Identify the blood parasite species.
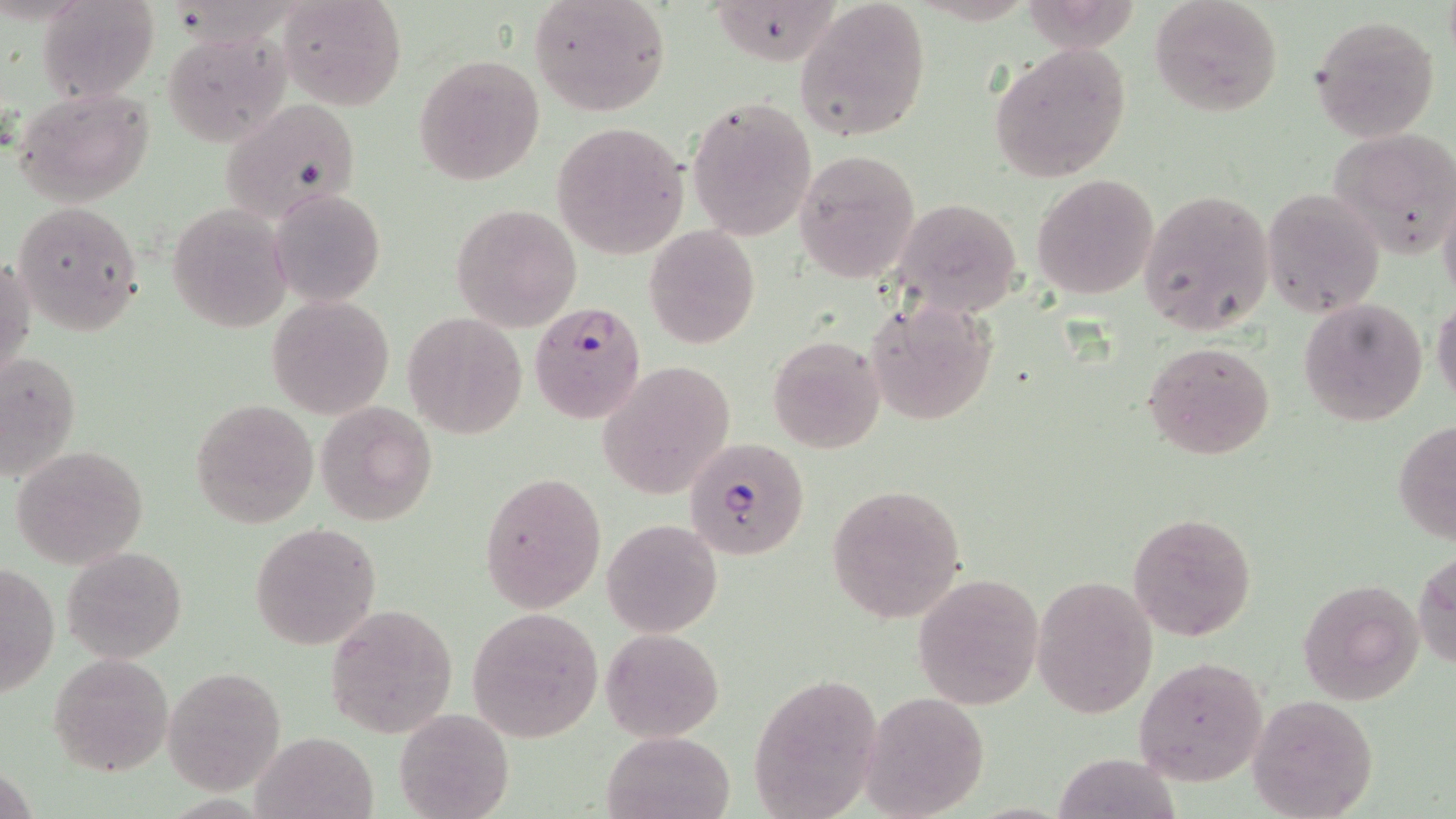
Plasmodium falciparum.

Approximate bounding boxes as [x1, y1, x2, y2] in pixels. Plasmodium falciparum-infected red blood cell locations: [529, 301, 648, 423], [686, 436, 811, 558]. Uninfected red blood cell locations: [280, 0, 406, 112], [528, 0, 673, 116], [793, 0, 931, 142], [1149, 0, 1284, 117], [38, 2, 156, 101], [1310, 16, 1440, 141], [163, 31, 289, 147], [989, 40, 1133, 182], [413, 54, 545, 185], [12, 86, 156, 207], [685, 97, 815, 241], [220, 98, 365, 223], [552, 124, 688, 257], [1327, 127, 1456, 258], [794, 149, 922, 284], [1031, 173, 1159, 300], [270, 188, 386, 307], [1262, 188, 1385, 314], [1138, 189, 1274, 336], [892, 198, 1023, 317], [12, 200, 145, 335], [167, 204, 292, 332], [451, 204, 582, 331], [644, 225, 760, 348], [1, 253, 35, 389], [267, 295, 395, 418], [1298, 297, 1428, 427], [1431, 297, 1456, 410], [865, 298, 995, 425], [402, 312, 527, 439], [767, 335, 887, 455], [1142, 340, 1276, 459], [1, 351, 80, 481], [596, 361, 737, 498], [190, 400, 320, 527], [315, 401, 436, 525], [1393, 420, 1456, 545], [12, 444, 148, 568], [479, 471, 607, 613], [828, 485, 968, 623], [1127, 512, 1257, 641], [601, 518, 722, 638], [249, 523, 382, 650], [63, 544, 186, 663], [1416, 547, 1456, 673], [0, 561, 58, 698], [912, 573, 1044, 709], [1297, 574, 1425, 704], [1032, 576, 1159, 719], [324, 603, 458, 740], [466, 608, 602, 741], [600, 628, 724, 742], [48, 651, 175, 778], [1133, 656, 1269, 786], [163, 667, 287, 792], [750, 672, 880, 819], [864, 692, 990, 818], [1246, 692, 1380, 818], [394, 708, 513, 819], [603, 730, 734, 819], [254, 731, 379, 819]. Image is 1456×819 pixels. May-Grünwald-Giemsa-stained preparation. Single field of view. Captured at 1000x magnification. Thin blood film. Optical microscopy.